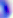

Summary:
  - Magnification: 400x
  - Identification: Toxoplasma gondii
  - Modality: photomicrograph